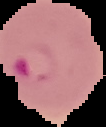
Cell region segmented out of the field of view; the surrounding area is masked to black. Image is 106×127 pixels. From a thin blood film. Malaria status: parasitized.